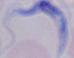

magnification = 1000x
identification = trypanosome
modality = photomicrograph